Identify the blood parasite species.
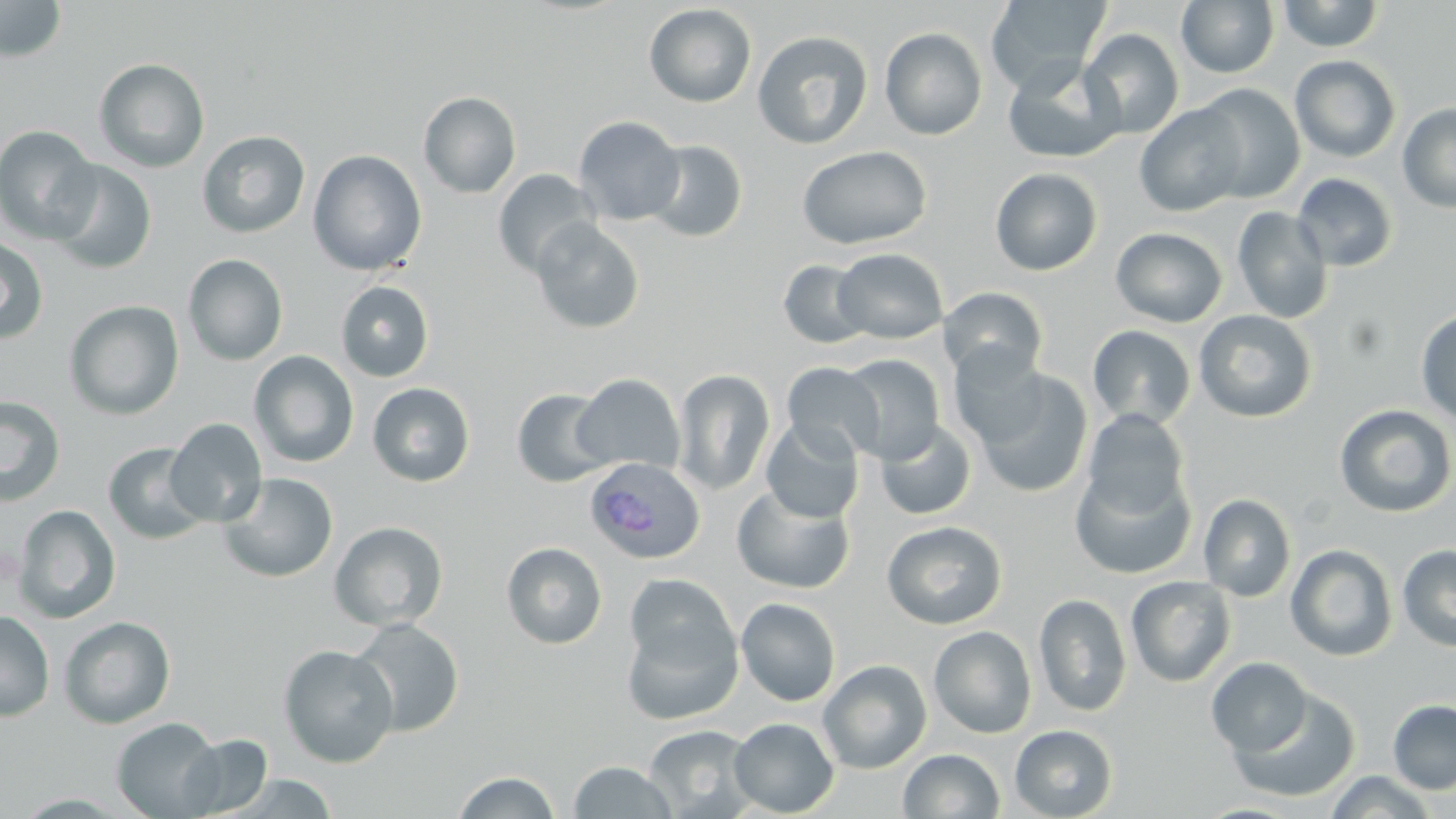
Plasmodium ovale.

Approximate bounding boxes as (x1,y1)-(x2,y2) corner pairs in pixels. Plasmodium ovale-infected red blood cell locations: (584,458)-(705,563). Uninfected red blood cell locations: (0,0)-(67,63), (986,0)-(1111,91), (1177,0)-(1279,78), (1276,0)-(1385,52), (643,3)-(757,108), (879,27)-(988,140), (1080,28)-(1185,139), (752,30)-(873,149), (1290,55)-(1401,163), (93,58)-(210,173), (1003,59)-(1125,163), (1194,83)-(1306,204), (419,90)-(521,198), (1397,103)-(1456,213), (1134,104)-(1248,217), (574,115)-(685,225), (0,125)-(100,244), (197,130)-(310,239), (643,139)-(748,243), (797,145)-(932,250), (307,150)-(427,276), (46,159)-(157,275), (990,167)-(1103,276), (492,169)-(601,278), (1292,173)-(1398,272), (1232,206)-(1334,324), (530,218)-(645,334), (1110,227)-(1228,328), (0,235)-(49,343), (832,248)-(948,344), (182,253)-(289,366), (778,259)-(873,348), (336,280)-(435,382), (939,287)-(1049,384), (63,299)-(184,420), (1415,308)-(1456,425), (1194,309)-(1317,423), (1087,324)-(1197,430), (948,343)-(1049,448), (248,350)-(359,468), (839,354)-(946,463), (782,362)-(884,462), (673,369)-(776,496), (974,370)-(1094,498), (571,374)-(685,475), (368,382)-(475,486), (511,388)-(615,487), (0,395)-(66,507), (1334,404)-(1455,517), (1080,409)-(1192,521), (165,418)-(268,527), (760,419)-(864,524), (875,419)-(977,520), (103,442)-(212,545), (1071,463)-(1197,578), (218,472)-(338,582), (731,484)-(855,595), (1198,493)-(1296,602), (13,505)-(121,624), (881,520)-(1007,629), (329,521)-(448,632), (501,541)-(608,649), (1285,544)-(1398,661), (1397,545)-(1456,651), (624,574)-(737,676), (1126,576)-(1237,687), (1034,593)-(1132,717), (736,597)-(841,706), (0,610)-(55,722), (621,611)-(743,726), (58,616)-(176,729), (347,618)-(464,737), (928,626)-(1037,738), (278,644)-(398,767), (1206,657)-(1312,756), (818,659)-(932,773), (1227,689)-(1362,803), (1387,699)-(1456,793), (111,717)-(224,818), (729,717)-(839,817), (643,724)-(759,818), (1009,724)-(1118,819), (179,733)-(274,817), (898,749)-(1004,818), (567,760)-(678,818), (452,770)-(562,818), (1323,771)-(1440,818), (222,773)-(339,818). Single field of view. Light microscopy. 1000x magnification. May-Grünwald-Giemsa-stained preparation. Image is 1456×819 pixels. Thin blood smear.